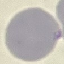
Malaria status: uninfected. Thin smear of blood. Giemsa stain. Photographed with a smartphone camera at the microscope eyepiece. Automatically extracted cell patch, resized to 64 × 64 pixels.